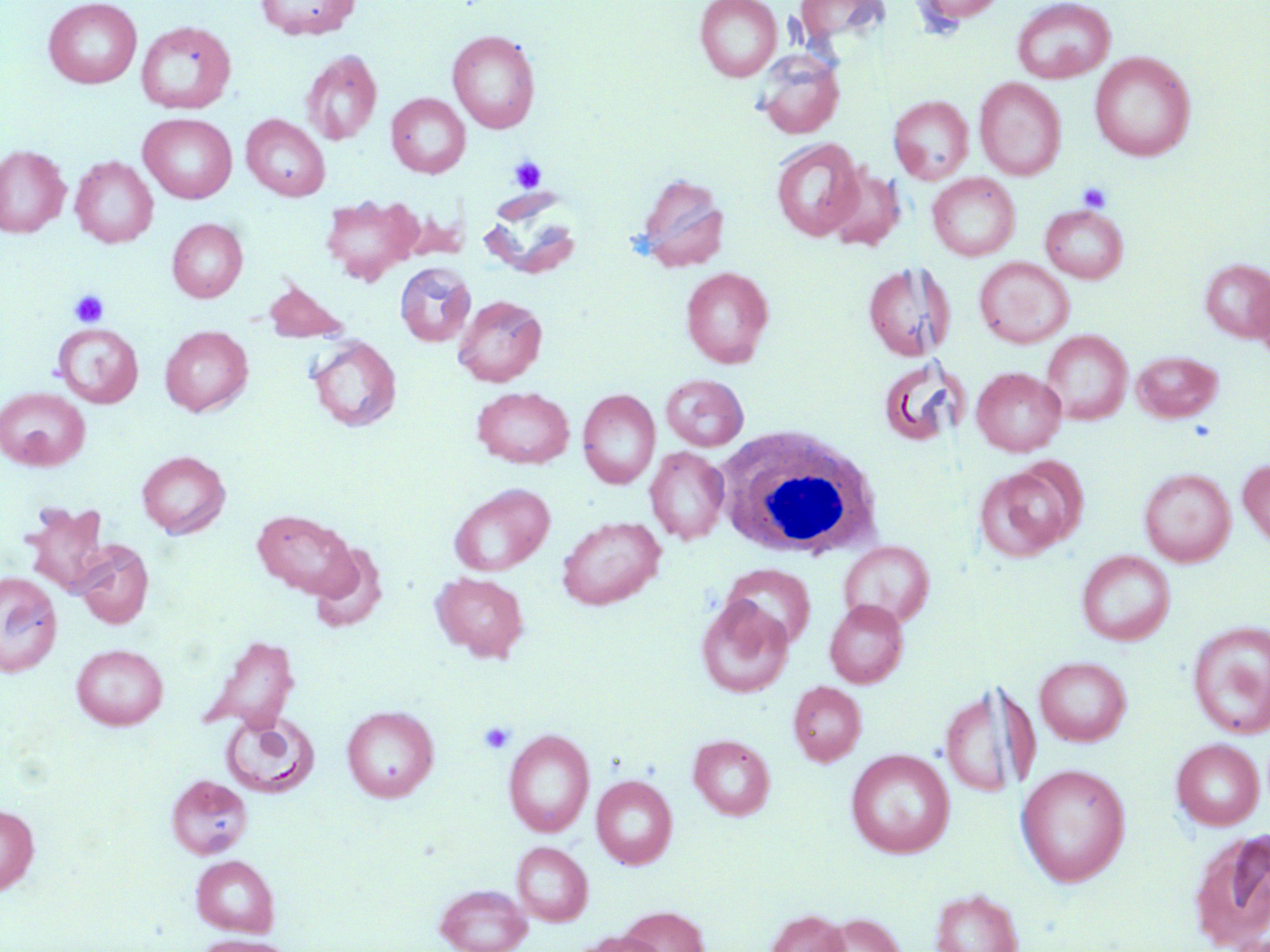

Summary:
  - Coordinate format: approximate bounding boxes as named x1/y1/x2/y2 corners in pixels
  - White blood cell locations: (x1=716, y1=425, x2=884, y2=560)
  - Platelet locations: (x1=508, y1=155, x2=547, y2=193), (x1=1077, y1=182, x2=1112, y2=213), (x1=69, y1=290, x2=109, y2=328), (x1=478, y1=721, x2=516, y2=756)
  - Uninfected red blood cell locations: (x1=43, y1=0, x2=142, y2=89), (x1=255, y1=0, x2=360, y2=39), (x1=695, y1=0, x2=781, y2=81), (x1=795, y1=0, x2=888, y2=47), (x1=913, y1=0, x2=1008, y2=25), (x1=1011, y1=0, x2=1116, y2=83), (x1=136, y1=20, x2=236, y2=114), (x1=447, y1=29, x2=541, y2=133), (x1=300, y1=50, x2=382, y2=146), (x1=754, y1=51, x2=845, y2=139), (x1=1089, y1=52, x2=1196, y2=161), (x1=974, y1=77, x2=1067, y2=180), (x1=386, y1=93, x2=470, y2=178), (x1=888, y1=95, x2=973, y2=184), (x1=138, y1=113, x2=237, y2=203), (x1=241, y1=114, x2=330, y2=201), (x1=770, y1=137, x2=864, y2=241), (x1=0, y1=146, x2=70, y2=237), (x1=70, y1=156, x2=158, y2=247), (x1=825, y1=167, x2=906, y2=251), (x1=635, y1=173, x2=731, y2=272), (x1=927, y1=173, x2=1020, y2=261), (x1=320, y1=193, x2=423, y2=285), (x1=1041, y1=204, x2=1128, y2=283), (x1=167, y1=219, x2=247, y2=302), (x1=975, y1=257, x2=1074, y2=348), (x1=1200, y1=259, x2=1270, y2=342), (x1=395, y1=262, x2=476, y2=347), (x1=863, y1=262, x2=955, y2=361), (x1=681, y1=266, x2=773, y2=367), (x1=1251, y1=272, x2=1270, y2=360), (x1=261, y1=279, x2=350, y2=343), (x1=453, y1=295, x2=547, y2=386), (x1=53, y1=323, x2=143, y2=407), (x1=160, y1=325, x2=253, y2=416), (x1=1042, y1=330, x2=1131, y2=424), (x1=306, y1=335, x2=402, y2=432), (x1=1133, y1=351, x2=1223, y2=423), (x1=876, y1=357, x2=968, y2=448), (x1=972, y1=367, x2=1066, y2=456), (x1=661, y1=374, x2=749, y2=451), (x1=472, y1=386, x2=574, y2=469), (x1=0, y1=387, x2=90, y2=470), (x1=578, y1=389, x2=660, y2=489), (x1=645, y1=446, x2=729, y2=545), (x1=136, y1=450, x2=231, y2=538), (x1=1237, y1=458, x2=1270, y2=550), (x1=974, y1=463, x2=1082, y2=561), (x1=1138, y1=468, x2=1236, y2=566), (x1=449, y1=483, x2=555, y2=576), (x1=21, y1=501, x2=110, y2=595), (x1=252, y1=509, x2=357, y2=598), (x1=557, y1=515, x2=665, y2=610), (x1=73, y1=540, x2=154, y2=628), (x1=838, y1=540, x2=935, y2=628), (x1=308, y1=544, x2=387, y2=632), (x1=1076, y1=550, x2=1175, y2=646), (x1=722, y1=564, x2=815, y2=650), (x1=0, y1=571, x2=63, y2=676), (x1=431, y1=572, x2=529, y2=662), (x1=696, y1=596, x2=793, y2=698), (x1=824, y1=600, x2=909, y2=688), (x1=1187, y1=621, x2=1270, y2=739), (x1=200, y1=635, x2=300, y2=734), (x1=71, y1=643, x2=169, y2=730), (x1=1035, y1=656, x2=1132, y2=746), (x1=788, y1=681, x2=867, y2=766), (x1=938, y1=681, x2=1035, y2=800), (x1=341, y1=705, x2=439, y2=802), (x1=221, y1=710, x2=320, y2=797), (x1=503, y1=728, x2=595, y2=837), (x1=688, y1=735, x2=775, y2=820), (x1=1171, y1=738, x2=1265, y2=830), (x1=846, y1=749, x2=955, y2=858), (x1=1016, y1=763, x2=1131, y2=886), (x1=591, y1=774, x2=677, y2=869), (x1=166, y1=776, x2=252, y2=858), (x1=0, y1=804, x2=39, y2=895), (x1=1189, y1=828, x2=1270, y2=952), (x1=511, y1=841, x2=593, y2=926), (x1=191, y1=855, x2=279, y2=937), (x1=435, y1=883, x2=532, y2=952), (x1=930, y1=888, x2=1024, y2=952), (x1=619, y1=907, x2=710, y2=952), (x1=765, y1=910, x2=849, y2=952), (x1=816, y1=913, x2=906, y2=952), (x1=571, y1=931, x2=665, y2=952), (x1=194, y1=935, x2=296, y2=952)
  - Slide-level diagnosis: no evidence of blood parasites
  - Stain: May-Grünwald-Giemsa
  - Image size: 1270×952 pixels
  - Field of view: single
  - Modality: light microscopy
  - Preparation: thin blood film
  - Magnification: 1000x